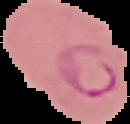

Summary:
  - Preparation: thin blood film
  - Image type: segmented cell region with the area outside set to black
  - Image size: 130×124 pixels
  - Result: Plasmodium parasites identified